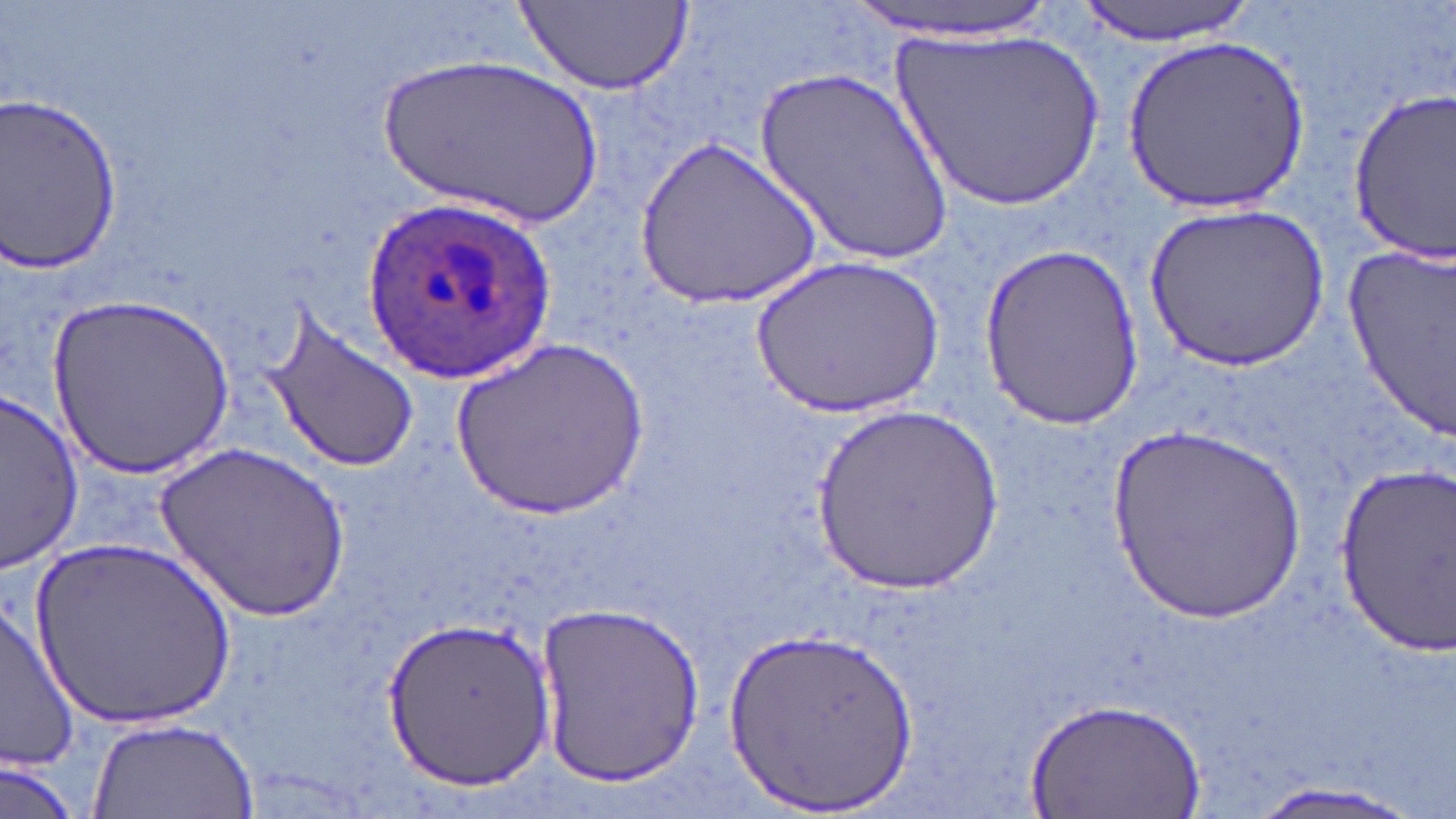

Summary:
  - Coordinate format: approximate bounding boxes as (x1, y1, x2, y2) in pixels
  - Uninfected red blood cell locations: (850, 0, 1059, 41), (1075, 0, 1260, 45), (518, 2, 689, 94), (887, 26, 1110, 212), (1123, 33, 1311, 211), (379, 53, 608, 230), (754, 67, 956, 270), (1344, 90, 1456, 262), (0, 97, 125, 271), (636, 133, 821, 310), (1145, 201, 1327, 374), (1341, 239, 1455, 440), (978, 242, 1143, 428), (752, 257, 940, 420), (49, 292, 235, 481), (260, 300, 421, 474), (446, 340, 648, 520), (1, 391, 83, 569), (809, 403, 1003, 597), (1110, 425, 1309, 625), (159, 441, 349, 625), (1330, 456, 1455, 656), (27, 539, 238, 733), (537, 599, 706, 789), (1, 604, 81, 772), (381, 614, 553, 790), (722, 624, 923, 819), (1028, 699, 1205, 819), (89, 717, 261, 819), (1, 756, 80, 819), (1240, 782, 1429, 819)
  - Plasmodium ovale-infected red blood cell locations: (360, 195, 557, 380)
  - Slide-level diagnosis: Plasmodium ovale
  - Image size: 1456×819 pixels
  - Field of view: one of a larger specimen
  - Stain: May-Grünwald-Giemsa
  - Magnification: 1000x
  - Modality: light microscopy
  - Preparation: thin blood film